State which parasite is depicted.
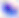
This is Toxoplasma gondii.

Photomicrograph. 400x magnification.